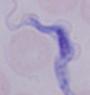
Captured at 1000x magnification. A trypanosome is shown. Photomicrograph.